Report the malaria status of this cell.
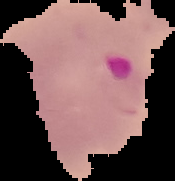

It is parasitized.

Image is 175×181 pixels. The area outside the segmented cell region is set to black. From a thin blood film.